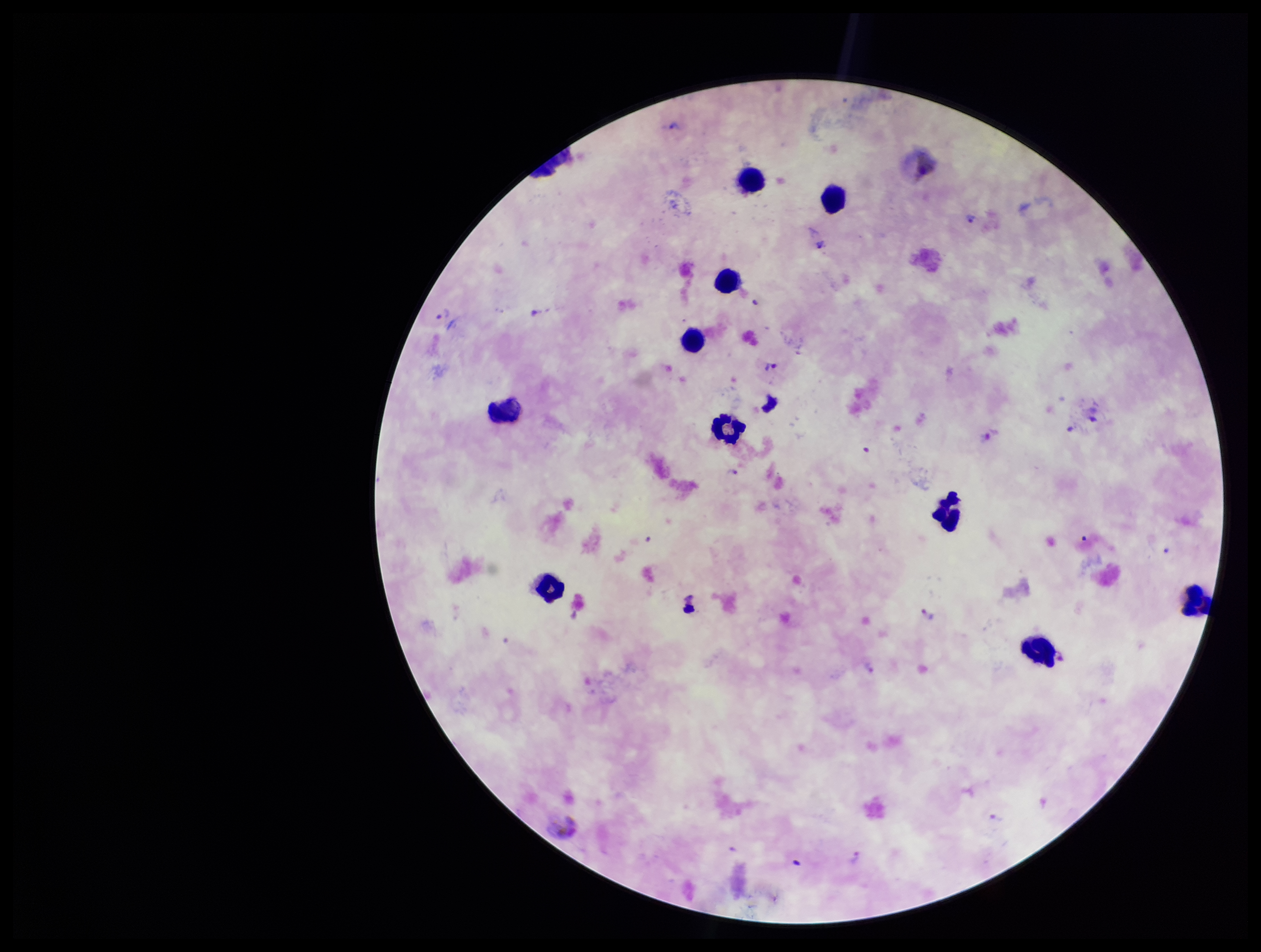 Parasite count: 6. Photographed through the microscope eyepiece with a smartphone camera. Image is 1261×952 pixels. Species reported for this patient: Plasmodium vivax. Giemsa stain. Single field of view. Leukocyte count: 10. Preparation: thick. Patient malaria status: positive. Plasmodium parasites: identified.